Comment on the morphology of the red blood cells.
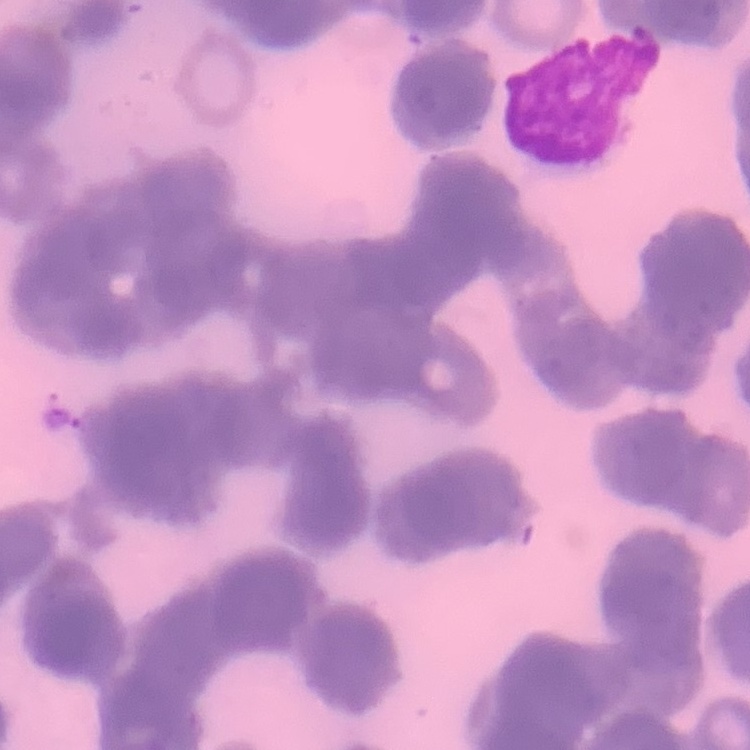
They show rouleaux formation.

preparation = thin peripheral smear
stain = Field's or Giemsa
image type = square crop of a larger photomicrograph